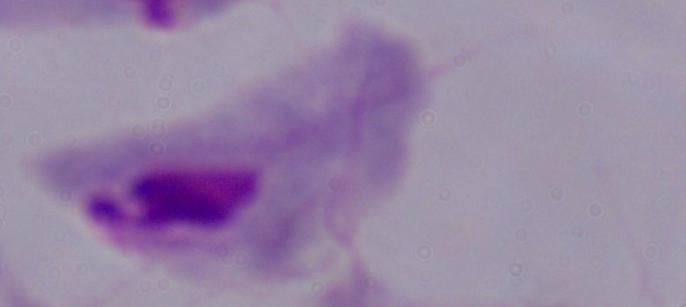

Summary:
  - Magnification: 1000x
  - Identification: trichomonad
  - Modality: photomicrograph